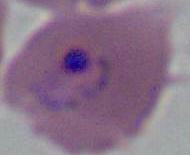 Micrograph. Captured at either 400x or 1000x magnification. A Plasmodium parasite is shown.